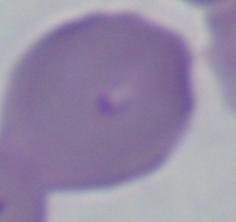

identification = Babesia
magnification = 1000x
modality = micrograph